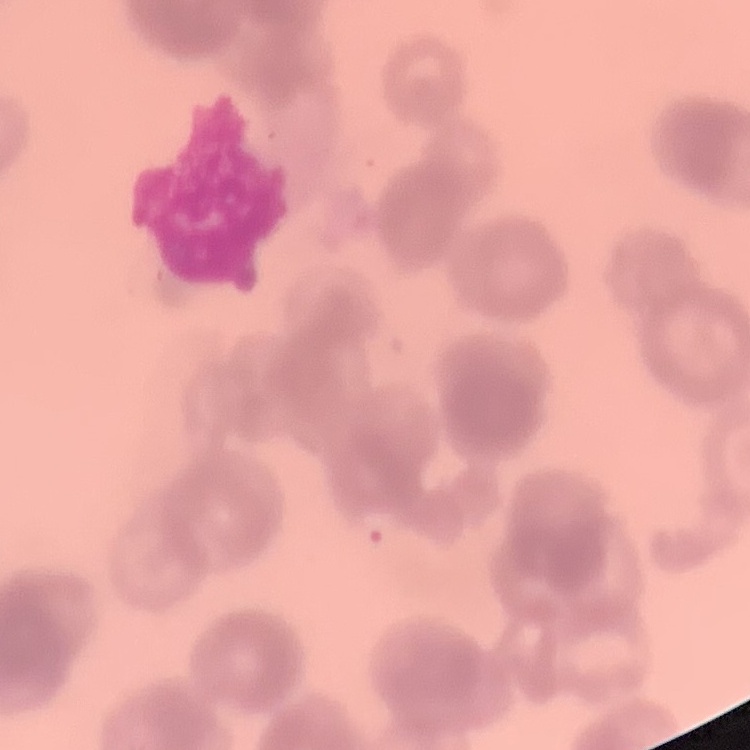

Summary:
  - Red blood cell morphology: rouleaux formation
  - Preparation: thin blood smear
  - Stain: Field's or Giemsa
  - Image type: one tile cut from a larger photomicrograph